Name the parasite shown.
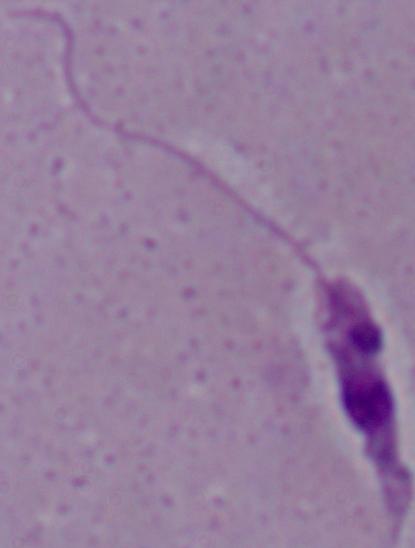
This is Leishmania.

modality = micrograph
magnification = 1000x